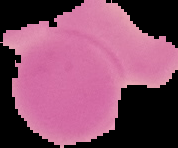

Summary:
  - Image size: 178×148 pixels
  - Result: no malaria parasites seen
  - Preparation: thin blood film
  - Image type: segmented cell region on a black background